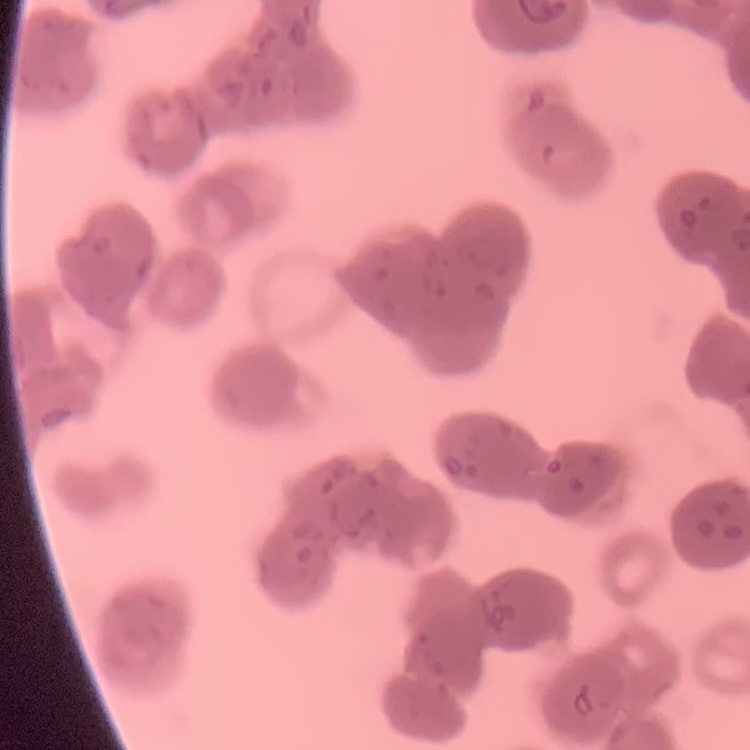

The red blood cells exhibit rouleaux formation. Field's or Giemsa stain. Thin blood smear. Square crop of a larger photomicrograph.